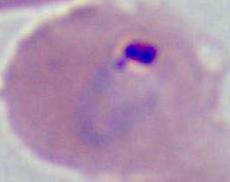

{
  "modality": "micrograph",
  "magnification": "400x or 1000x",
  "identification": "Plasmodium"
}